Assess this cell for malaria.
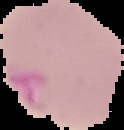
Parasitized.

Summary:
  - Preparation: thin blood smear
  - Image size: 124×130 pixels
  - Image type: segmented cell region on a black background